Evaluate for parasitized red blood cells.
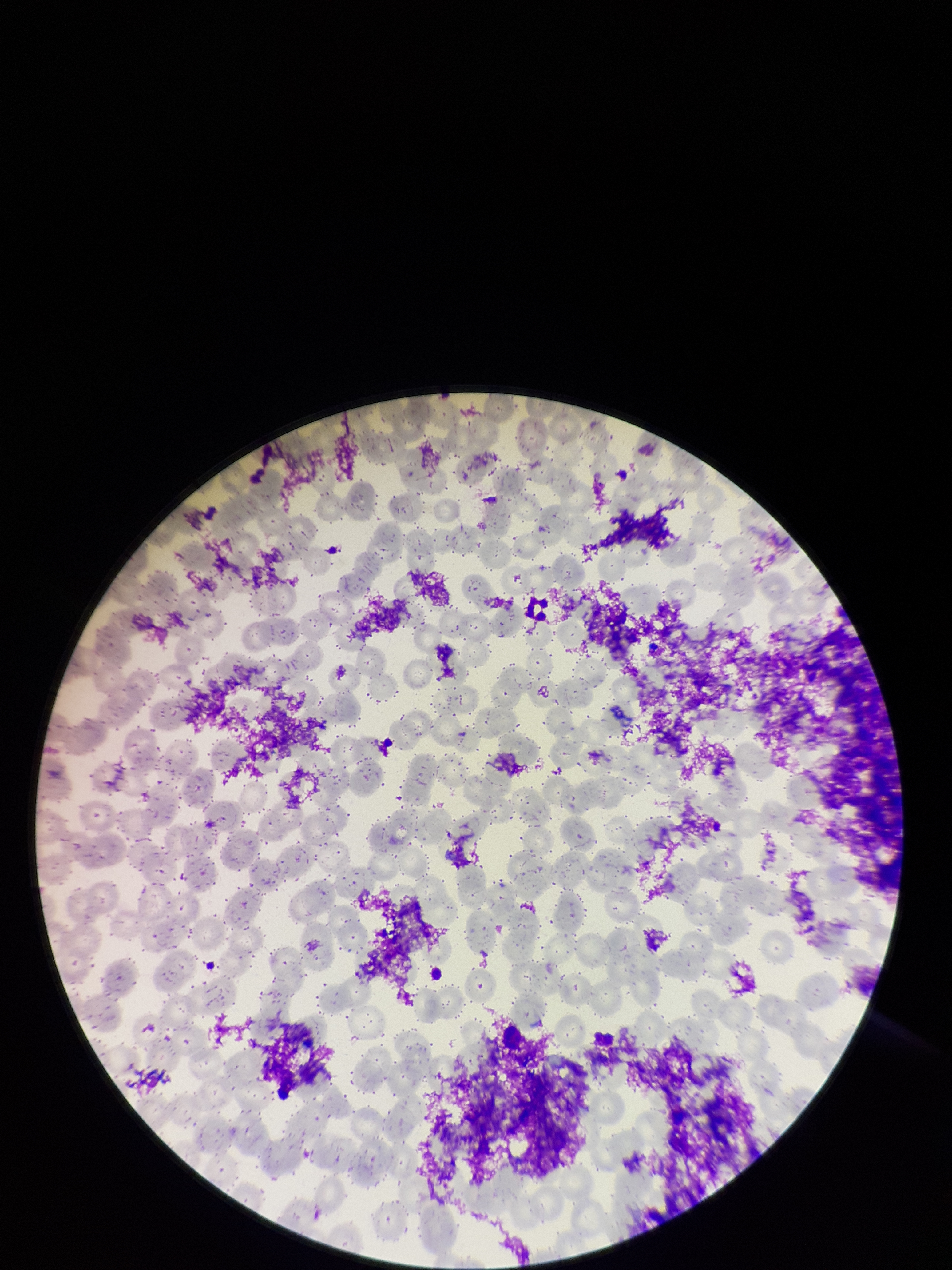

None detected.

image size = 952×1270 pixels
capture = smartphone photograph through the microscope eyepiece
red blood cell count = 299
parasitized red blood cell count = 0
patient malaria status = negative
stain = Giemsa
preparation = thin smear
field of view = one from this slide